Identify the blood parasite species.
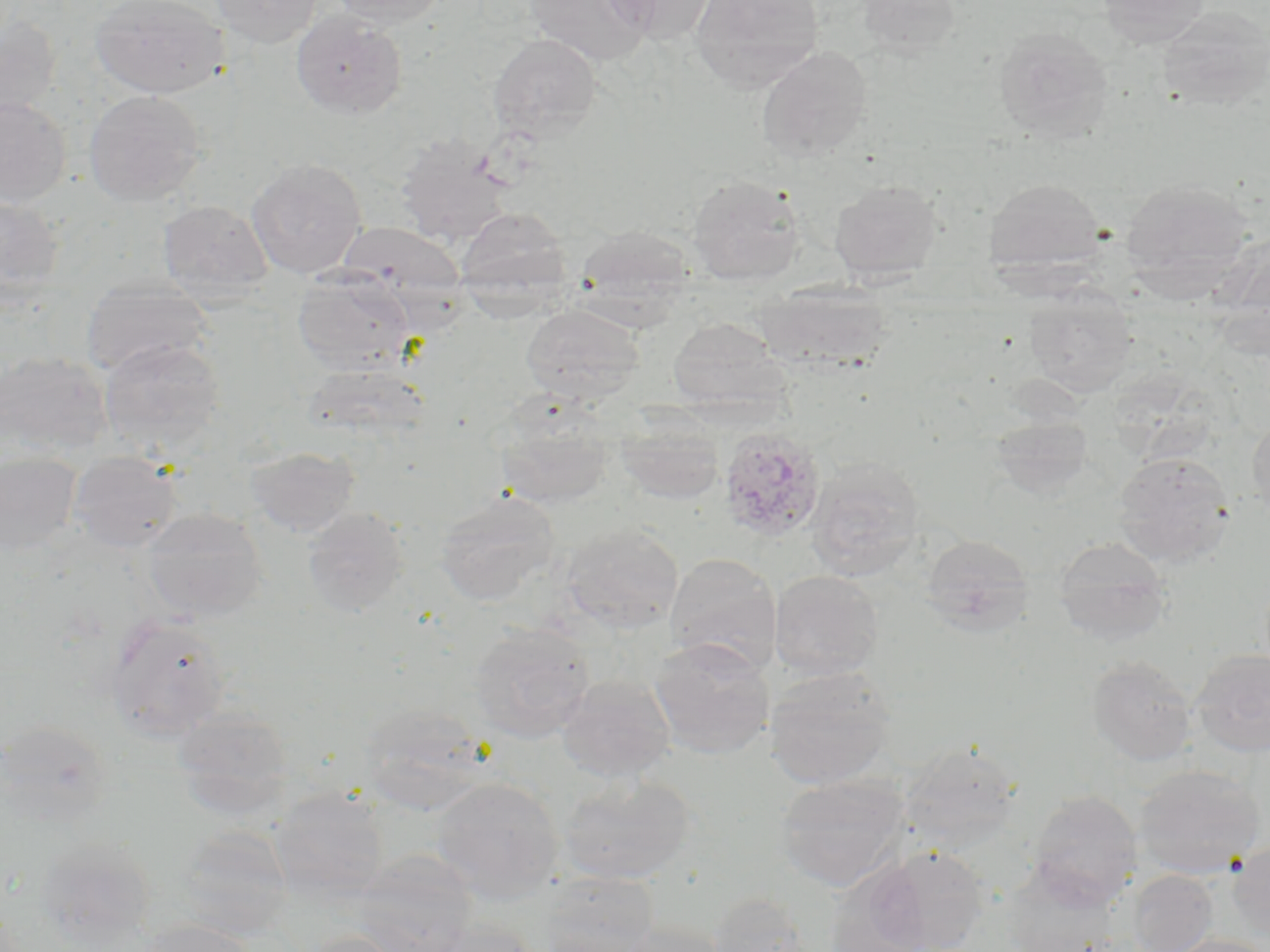
Plasmodium ovale.

modality = light microscopy
stain = May-Grünwald-Giemsa
magnification = 1000x
Plasmodium ovale-infected red blood cell locations = approximate bounding boxes as named x1/y1/x2/y2 corners in pixels: (x1=718, y1=426, x2=827, y2=543)
uninfected red blood cell locations = approximate bounding boxes as named x1/y1/x2/y2 corners in pixels: (x1=89, y1=0, x2=229, y2=99), (x1=209, y1=0, x2=323, y2=48), (x1=325, y1=0, x2=449, y2=28), (x1=600, y1=0, x2=718, y2=43), (x1=690, y1=0, x2=825, y2=91), (x1=856, y1=0, x2=962, y2=57), (x1=1096, y1=0, x2=1210, y2=47), (x1=524, y1=1, x2=655, y2=67), (x1=1155, y1=6, x2=1270, y2=112), (x1=290, y1=10, x2=408, y2=119), (x1=0, y1=13, x2=62, y2=126), (x1=993, y1=27, x2=1114, y2=143), (x1=488, y1=32, x2=602, y2=142), (x1=756, y1=46, x2=873, y2=162), (x1=84, y1=89, x2=206, y2=206), (x1=0, y1=96, x2=71, y2=208), (x1=396, y1=135, x2=514, y2=248), (x1=246, y1=158, x2=367, y2=279), (x1=686, y1=174, x2=804, y2=285), (x1=1119, y1=177, x2=1254, y2=292), (x1=985, y1=178, x2=1106, y2=275), (x1=829, y1=179, x2=943, y2=283), (x1=0, y1=196, x2=65, y2=309), (x1=157, y1=200, x2=274, y2=303), (x1=454, y1=206, x2=575, y2=309), (x1=337, y1=221, x2=465, y2=306), (x1=576, y1=225, x2=693, y2=310), (x1=292, y1=269, x2=417, y2=375), (x1=81, y1=277, x2=214, y2=377), (x1=755, y1=282, x2=892, y2=373), (x1=1024, y1=285, x2=1137, y2=397), (x1=520, y1=303, x2=646, y2=404), (x1=668, y1=316, x2=788, y2=411), (x1=98, y1=338, x2=226, y2=454), (x1=0, y1=351, x2=112, y2=458), (x1=302, y1=362, x2=431, y2=446), (x1=494, y1=395, x2=617, y2=508), (x1=615, y1=411, x2=724, y2=505), (x1=1246, y1=414, x2=1270, y2=521), (x1=990, y1=415, x2=1095, y2=501), (x1=245, y1=446, x2=360, y2=536), (x1=1112, y1=451, x2=1235, y2=567), (x1=0, y1=452, x2=82, y2=556), (x1=68, y1=452, x2=183, y2=552), (x1=805, y1=457, x2=925, y2=579), (x1=434, y1=489, x2=560, y2=605), (x1=142, y1=507, x2=267, y2=621), (x1=302, y1=507, x2=409, y2=617), (x1=561, y1=523, x2=685, y2=633), (x1=921, y1=534, x2=1034, y2=637), (x1=1053, y1=536, x2=1171, y2=645), (x1=665, y1=553, x2=781, y2=674), (x1=769, y1=569, x2=883, y2=680), (x1=104, y1=613, x2=232, y2=742), (x1=468, y1=622, x2=596, y2=742), (x1=648, y1=637, x2=775, y2=758), (x1=1190, y1=649, x2=1270, y2=757), (x1=1086, y1=655, x2=1197, y2=766), (x1=764, y1=666, x2=896, y2=789), (x1=557, y1=674, x2=675, y2=782), (x1=357, y1=704, x2=492, y2=816), (x1=172, y1=705, x2=293, y2=821), (x1=0, y1=720, x2=112, y2=827), (x1=899, y1=742, x2=1022, y2=851), (x1=1134, y1=764, x2=1265, y2=879), (x1=558, y1=773, x2=696, y2=886), (x1=774, y1=773, x2=910, y2=892), (x1=431, y1=776, x2=564, y2=902), (x1=269, y1=787, x2=390, y2=903), (x1=1027, y1=789, x2=1143, y2=906), (x1=172, y1=826, x2=292, y2=938), (x1=36, y1=836, x2=156, y2=944), (x1=1228, y1=841, x2=1270, y2=941), (x1=867, y1=846, x2=990, y2=951), (x1=352, y1=851, x2=477, y2=952), (x1=821, y1=862, x2=935, y2=952), (x1=1004, y1=863, x2=1122, y2=951), (x1=1127, y1=869, x2=1217, y2=952), (x1=533, y1=871, x2=660, y2=952), (x1=707, y1=891, x2=818, y2=952), (x1=135, y1=919, x2=257, y2=952), (x1=421, y1=919, x2=544, y2=952), (x1=615, y1=920, x2=730, y2=952), (x1=300, y1=931, x2=408, y2=952), (x1=1162, y1=934, x2=1270, y2=952)
preparation = thin blood film
image size = 1270×952 pixels
field of view = single